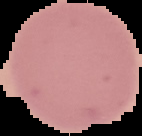

From a thin blood smear. Image is 142×136 pixels. The area outside the segmented cell region is set to black. Malaria status: uninfected.